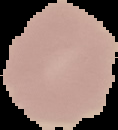
preparation = thin blood film
result = no Plasmodium parasites detected
image size = 118×130 pixels
image type = segmented cell region on a black background